Assess this cell for malaria.
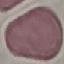

It is uninfected.

Automatically extracted cell patch, resized to 64 × 64 pixels. Thin blood film. Giemsa stain. Photographed with a smartphone camera at the microscope eyepiece.